Point out each malaria parasite and each leukocyte.
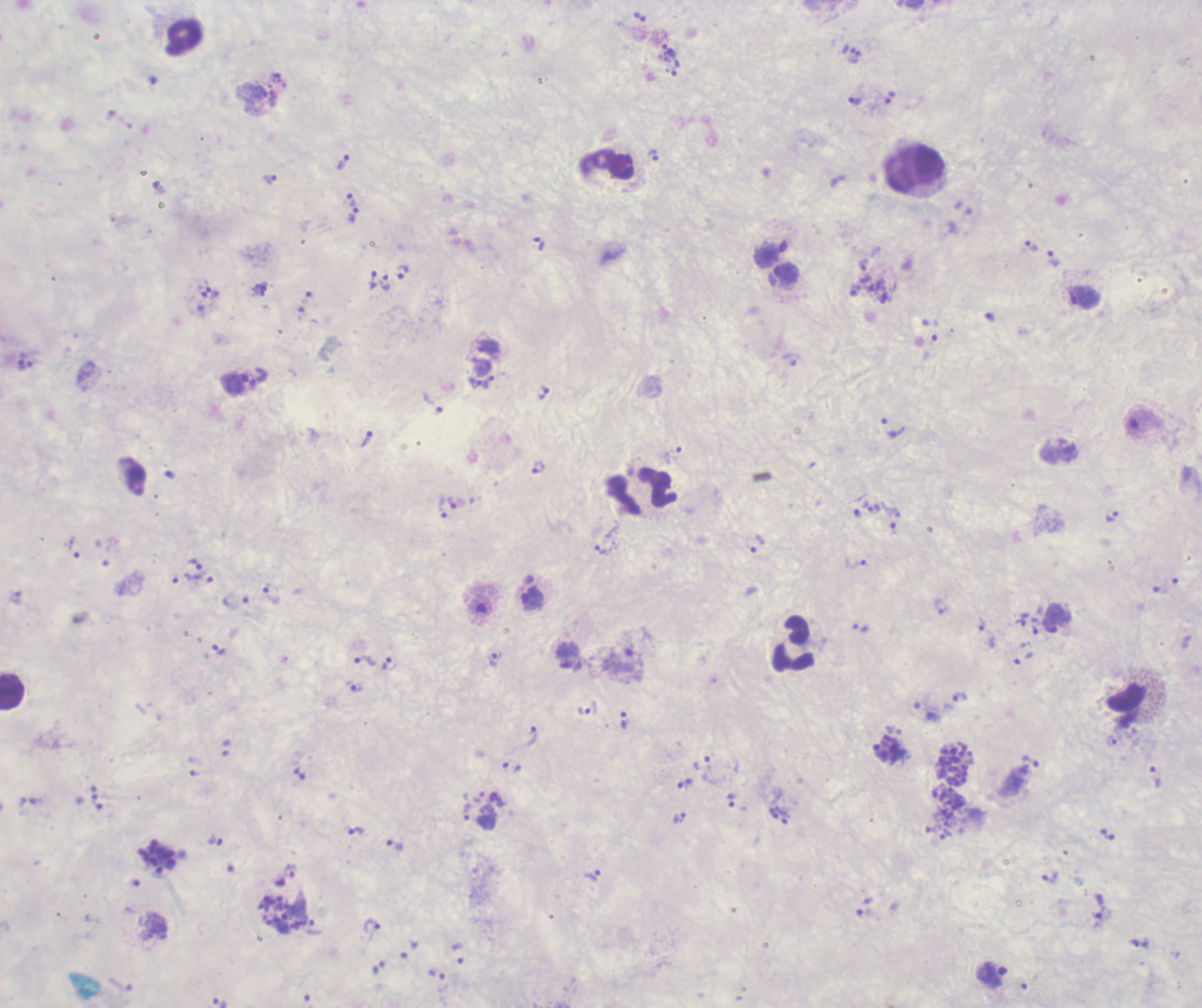

Approximate centers as {x, y} in pixels.
Trophozoites: {669, 51}, {855, 58}, {889, 97}, {854, 100}, {653, 155}, {343, 161}, {270, 179}, {350, 198}, {353, 214}, {538, 244}, {1032, 246}, {1053, 258}, {864, 264}, {402, 272}, {785, 274}, {373, 280}, {385, 283}, {877, 284}, {259, 290}, {212, 292}, {1084, 296}, {488, 382}, {474, 383}, {234, 384}, {543, 393}, {434, 405}, {892, 426}, {367, 438}, {673, 454}, {538, 467}, {443, 508}, {874, 508}, {890, 514}, {1112, 515}, {758, 543}, {74, 547}, {604, 549}, {856, 563}, {195, 564}, {199, 578}, {272, 593}, {533, 598}, {941, 607}, {986, 632}, {219, 649}, {567, 656}, {495, 659}, {620, 660}, {364, 661}, {389, 663}, {355, 687}, {960, 696}, {587, 708}, {532, 737}, {1031, 761}, {1155, 777}, {685, 783}, {731, 800}, {467, 811}, {680, 817}, {785, 817}, {356, 831}, {945, 834}, {1108, 834}, {216, 841}, {395, 844}, {593, 876}, {1049, 877}, {1100, 905}, {371, 925}, {993, 974}.
Schizonts: {954, 766}, {947, 804}, {158, 858}, {278, 916}.
No gametocyte forms observed.
Leukocytes: {184, 36}, {916, 169}, {642, 492}, {795, 644}, {12, 692}.

Summary:
  - Magnification: 100x
  - Preparation: thick smear of blood
  - Context: previously used in an actual diagnosis
  - Background quality: poor
  - Field of view: single
  - Image size: 1202×1008 pixels
  - Stain: Romanowsky
  - Coloration quality: bad